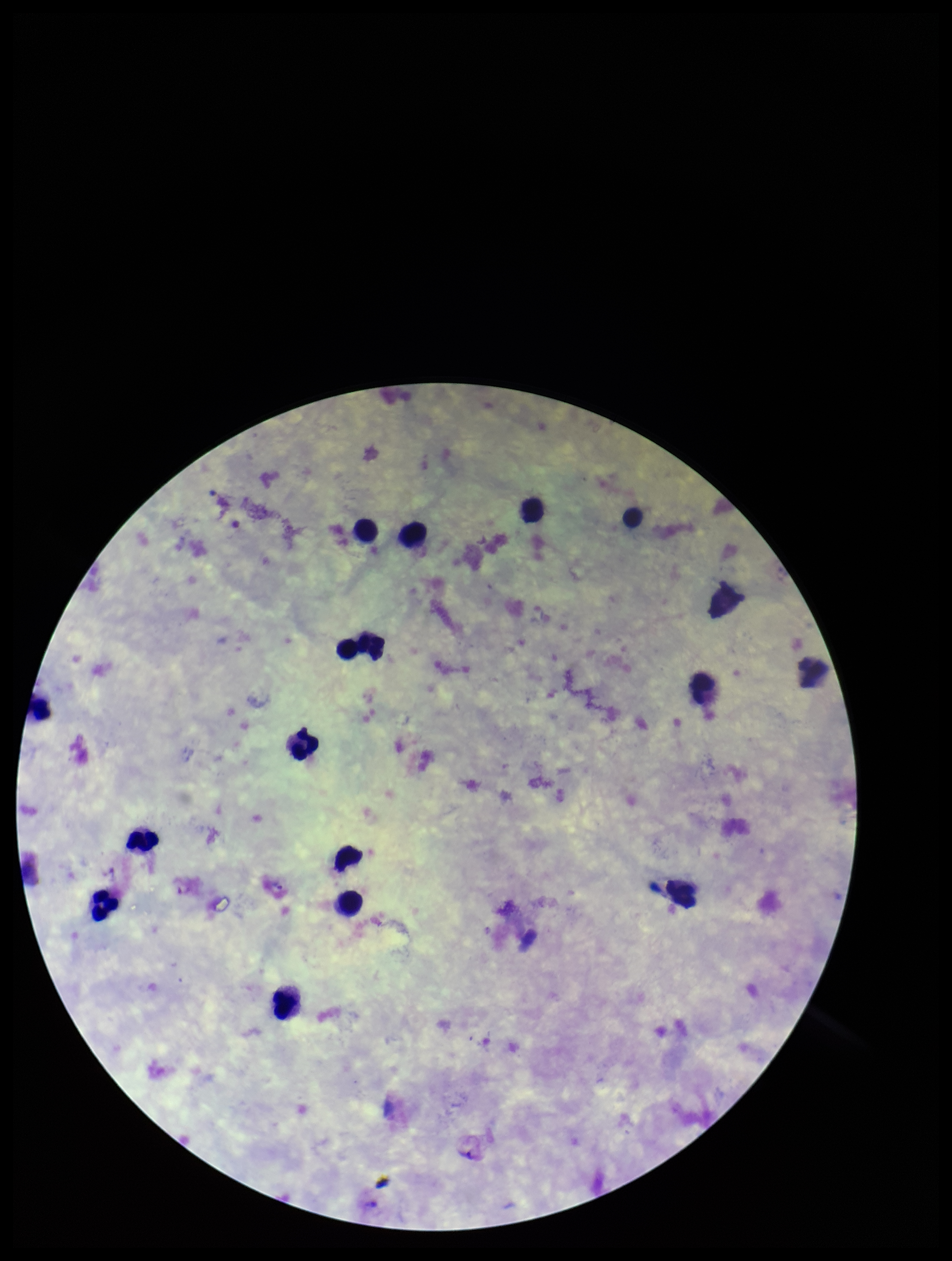

Summary:
  - Capture: smartphone photograph through the microscope eyepiece
  - Patient malaria status: positive
  - Field of view: one from this slide
  - Parasite count: 0
  - Leukocyte count: 15
  - Stain: Giemsa
  - Preparation: thick blood smear
  - Image size: 952×1261 pixels
  - Plasmodium parasites: none detected
  - Species reported for this patient: Plasmodium vivax